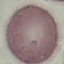
Malaria status: uninfected. Acquired by smartphone through the microscope eyepiece. Giemsa stain. Thin smear of blood. Cell patch, automatically extracted from a larger field of view and resized to 64 × 64 pixels.